Give the position of every Plasmodium parasite.
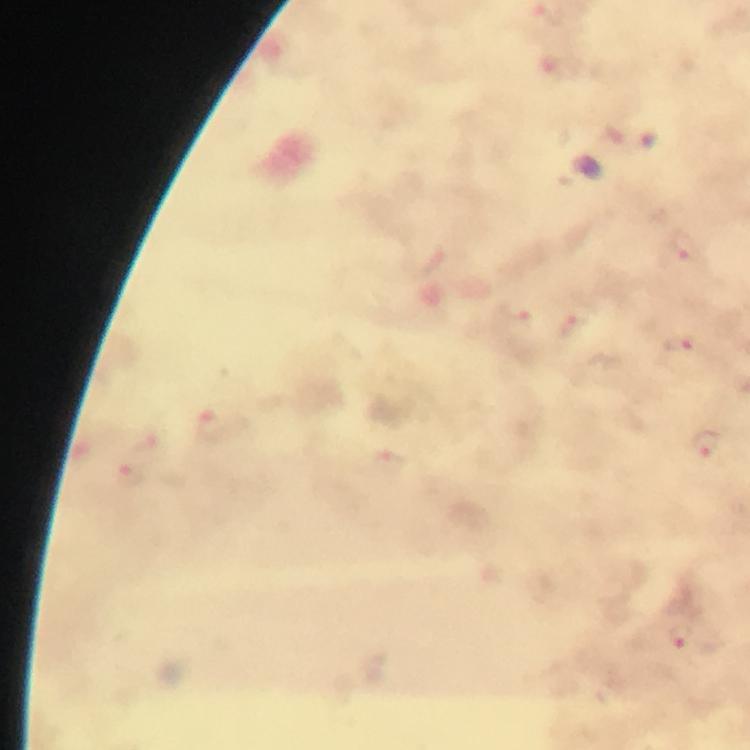
Approximate centers as [x, y] in pixels.
Plasmodium parasites: [685, 250], [574, 329], [678, 343], [705, 442], [681, 638].

context: from a malaria diagnostic workup
preparation: thick smear
stain: Giemsa
capture: smartphone photograph through a microscope
image_size: 750×750 pixels
magnification: 100x
cropped_from: a single field of view
immersion_oil: applied